Assess the morphology of the red blood cells.
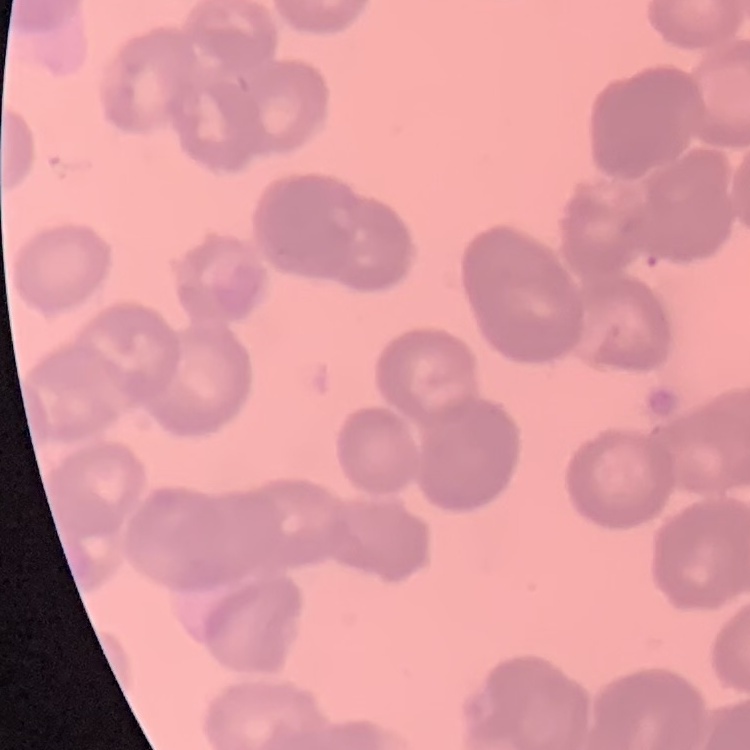

Rouleaux formation.

stain = Field's or Giemsa
image type = square crop of a larger photomicrograph
preparation = thin blood film